Describe the morphology of the red blood cells.
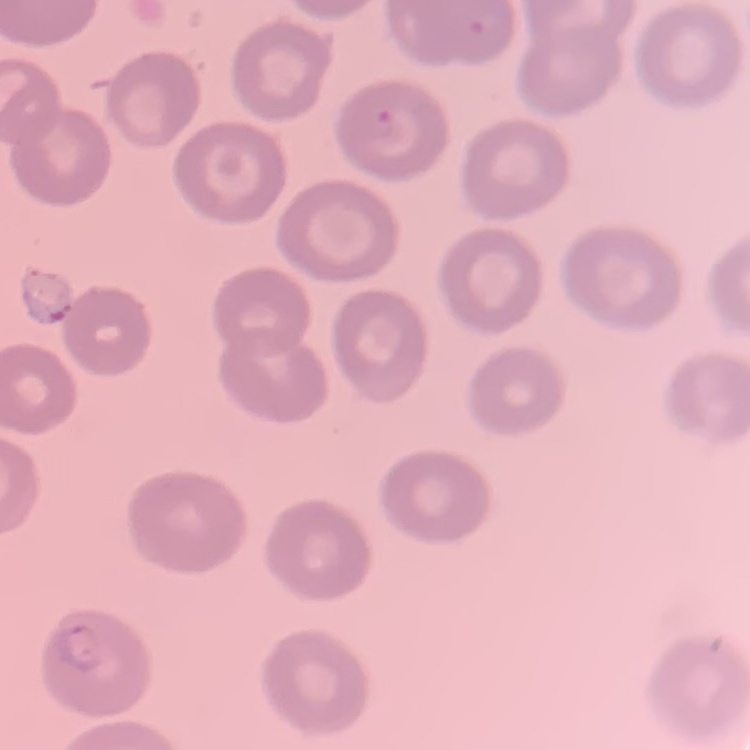
They show no rouleaux formation.

One tile cut from a larger photomicrograph. Thin peripheral smear. Stained with either Field's or Giemsa.